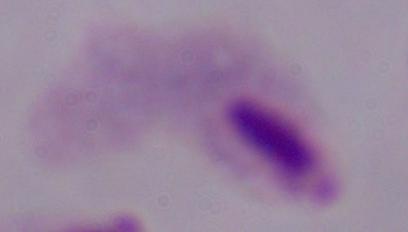
magnification = 1000x
identification = trichomonad
modality = micrograph